Identify the preparation type.
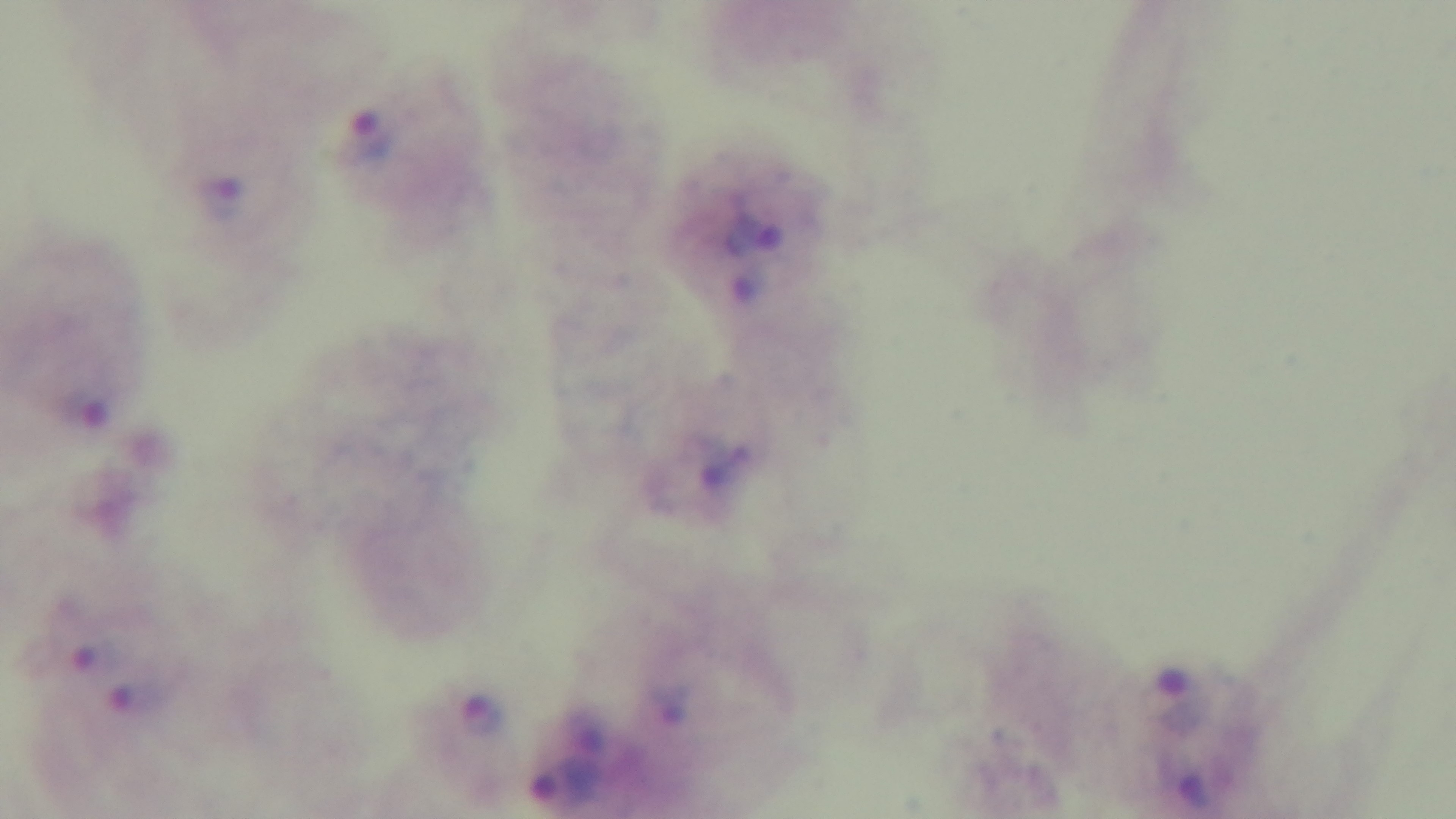

A thick smear.

Malaria status: infected. Captured with a mounted 4K digital camera. Light microscopy. 100x oil-immersion objective. Single field of view. Giemsa stain.